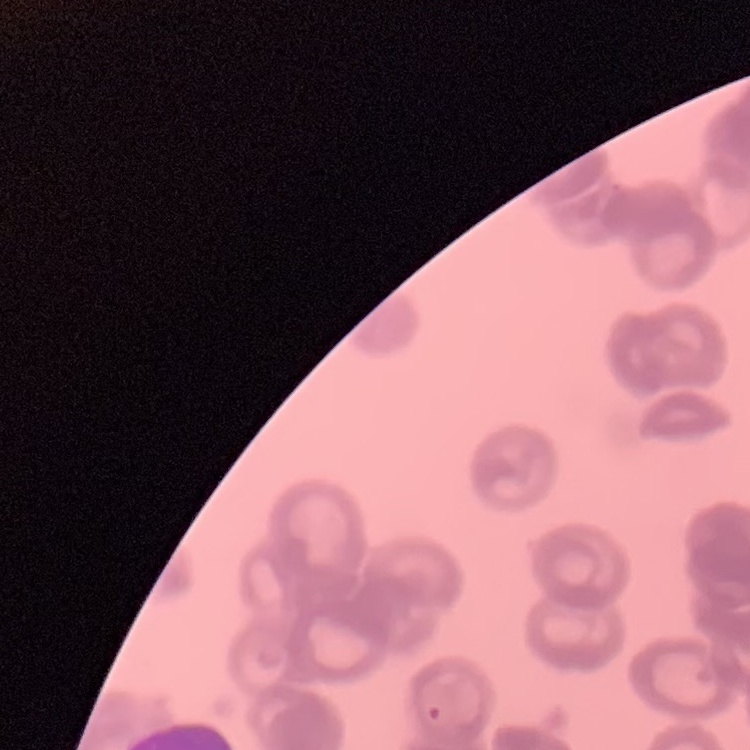
red_blood_cell_morphology: rouleaux formation
preparation: thin blood smear
image_type: one tile cut from a larger photomicrograph
stain: Field's or Giemsa